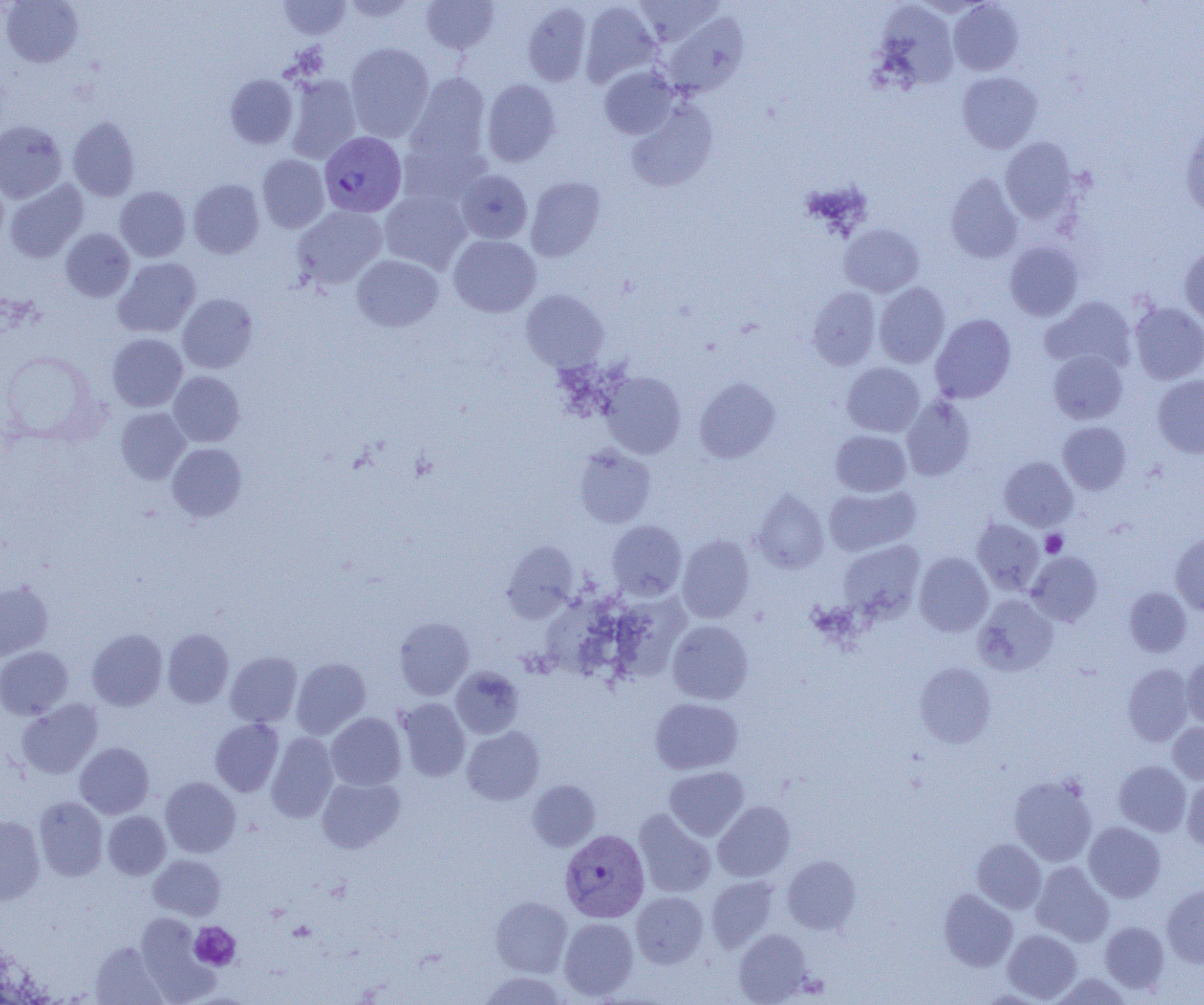
Approximate bounding boxes as (x1,y1)-(x2,y2) corner pairs in pixels. Plasmodium vivax-infected red blood cell locations: (319,131)-(406,217), (560,829)-(650,923). Platelet locations: (1041,530)-(1067,557), (190,921)-(241,970). Uninfected red blood cell locations: (1,0)-(83,67), (279,0)-(351,39), (341,0)-(418,22), (421,0)-(499,53), (634,0)-(723,47), (580,1)-(662,86), (874,1)-(960,91), (948,1)-(1023,76), (522,2)-(592,86), (665,11)-(748,96), (345,43)-(434,142), (599,66)-(679,139), (404,72)-(491,172), (957,72)-(1042,153), (225,74)-(298,148), (284,74)-(362,163), (482,78)-(561,167), (626,101)-(717,192), (68,117)-(139,200), (0,120)-(67,203), (1180,122)-(1204,218), (1000,137)-(1077,223), (257,154)-(329,233), (455,169)-(532,244), (946,172)-(1022,263), (0,174)-(8,251), (525,177)-(605,261), (188,179)-(264,258), (4,180)-(88,262), (115,186)-(190,262), (379,189)-(471,273), (292,205)-(387,289), (839,223)-(923,297), (61,228)-(135,302), (448,234)-(541,317), (1005,241)-(1083,321), (1179,245)-(1204,326), (351,254)-(443,332), (113,257)-(201,337), (874,282)-(951,368), (808,287)-(880,370), (521,289)-(608,371), (177,293)-(258,373), (1041,296)-(1136,373), (1130,302)-(1204,384), (930,314)-(1016,403), (107,333)-(187,411), (1,350)-(102,443), (1048,350)-(1127,424), (842,362)-(925,437), (168,371)-(244,447), (600,371)-(686,458), (1152,375)-(1204,458), (695,378)-(781,462), (901,396)-(975,481), (115,407)-(191,483), (1057,421)-(1131,494), (831,430)-(911,497), (167,442)-(247,521), (574,444)-(655,528), (999,457)-(1077,531), (824,484)-(921,556), (752,489)-(829,573), (972,518)-(1044,595), (606,520)-(686,600), (1171,532)-(1204,615), (677,535)-(754,623), (838,540)-(925,621), (502,541)-(580,622), (1027,551)-(1102,626), (914,552)-(993,636), (0,580)-(53,660), (1124,587)-(1192,657), (544,593)-(618,673), (973,594)-(1058,676), (610,595)-(691,686), (394,616)-(474,700), (667,620)-(753,704), (162,628)-(234,708), (86,629)-(167,710), (0,646)-(73,719), (225,651)-(302,727), (1181,655)-(1204,728), (291,657)-(371,738), (915,663)-(996,747), (1123,663)-(1193,746), (451,666)-(523,738), (650,697)-(743,774), (396,698)-(470,782), (17,699)-(102,779), (326,712)-(406,790), (210,718)-(284,797), (1168,722)-(1204,784), (462,726)-(544,805), (266,732)-(338,822), (75,742)-(154,818), (1114,760)-(1191,836), (665,766)-(749,840), (1010,775)-(1097,866), (316,776)-(405,853), (160,777)-(240,857), (1182,779)-(1204,851), (527,780)-(600,851), (34,796)-(108,881), (713,801)-(795,882), (634,809)-(717,898), (103,811)-(170,879), (0,816)-(45,904), (1084,822)-(1165,902), (972,839)-(1046,913), (148,854)-(226,920), (782,856)-(861,934), (1031,861)-(1114,946), (706,876)-(778,951), (1162,883)-(1204,967), (938,888)-(1017,971), (631,891)-(708,968), (491,896)-(572,976), (135,913)-(218,1003), (559,917)-(638,1000), (1100,921)-(1169,994), (734,929)-(813,1004), (1002,929)-(1081,1002), (90,941)-(168,1005), (479,971)-(568,1005), (1051,972)-(1133,1005). Slide-level diagnosis: Plasmodium vivax. Image is 1204×1005 pixels. Thin blood smear. Light microscopy. 1000x magnification. Single field of view.